Name the parasite shown.
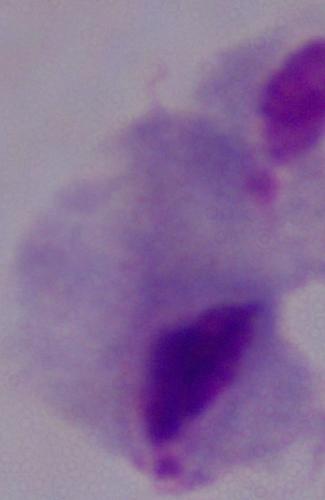
A trichomonad.

modality: micrograph
magnification: 1000x